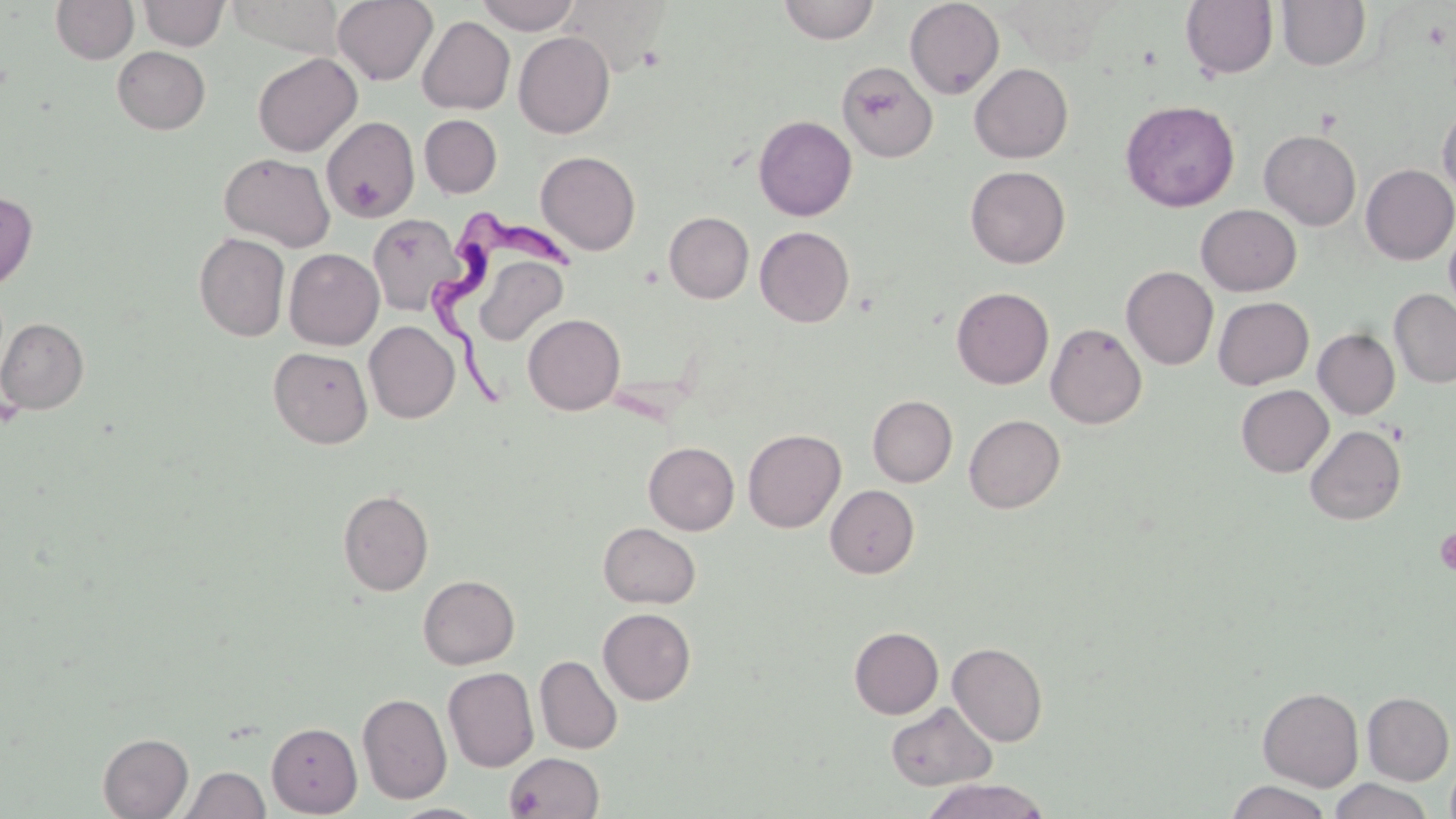
Approximate bounding boxes as [x1, y1, x2, y2] in pixels. Uninfected red blood cell locations: [51, 0, 139, 65], [138, 0, 229, 51], [225, 0, 345, 58], [332, 0, 438, 85], [475, 0, 580, 34], [559, 0, 671, 76], [904, 0, 1004, 99], [1181, 0, 1278, 79], [1276, 0, 1371, 71], [778, 1, 879, 44], [417, 16, 515, 114], [513, 32, 615, 138], [112, 46, 210, 134], [252, 52, 362, 156], [837, 61, 938, 162], [970, 63, 1073, 163], [1121, 100, 1239, 212], [1438, 103, 1456, 200], [419, 114, 502, 198], [321, 116, 419, 222], [753, 116, 857, 220], [1259, 130, 1361, 230], [536, 151, 640, 255], [219, 152, 335, 251], [1360, 164, 1456, 265], [965, 166, 1070, 268], [0, 191, 38, 290], [1196, 204, 1301, 296], [1205, 205, 1305, 390], [664, 212, 754, 303], [368, 213, 464, 315], [1444, 222, 1456, 319], [755, 226, 855, 327], [194, 232, 291, 341], [284, 248, 384, 350], [462, 249, 573, 347], [1121, 266, 1218, 370], [952, 287, 1053, 389], [1389, 289, 1456, 388], [1213, 296, 1313, 389], [523, 314, 625, 415], [0, 318, 89, 414], [364, 321, 460, 423], [1045, 322, 1147, 429], [1313, 329, 1400, 419], [269, 347, 373, 448], [1236, 385, 1333, 477], [868, 395, 957, 487], [964, 414, 1065, 513], [1304, 425, 1406, 525], [743, 428, 846, 532], [644, 442, 739, 535], [825, 485, 919, 578], [338, 489, 434, 596], [598, 522, 700, 608], [418, 575, 519, 669], [598, 608, 696, 705], [850, 627, 943, 719], [948, 642, 1048, 746], [535, 655, 622, 755], [443, 667, 539, 772], [1257, 687, 1364, 791], [357, 692, 452, 804], [1362, 692, 1454, 785], [886, 701, 996, 791], [266, 722, 362, 816], [98, 733, 193, 818], [504, 751, 604, 818], [1445, 758, 1456, 819], [179, 765, 270, 819], [920, 778, 1050, 819], [1329, 778, 1434, 819], [1226, 780, 1332, 819], [390, 803, 489, 819]. Platelet locations: [348, 174, 385, 218], [1434, 527, 1456, 578]. Trypanosoma brucei locations: [434, 211, 580, 420]. Slide-level diagnosis: Trypanosoma brucei. May-Grünwald-Giemsa stain. Image is 1456×819 pixels. Thin blood film. Optical microscopy. Captured at 1000x magnification. One field of a larger specimen.